Locate and identify every blood parasite.
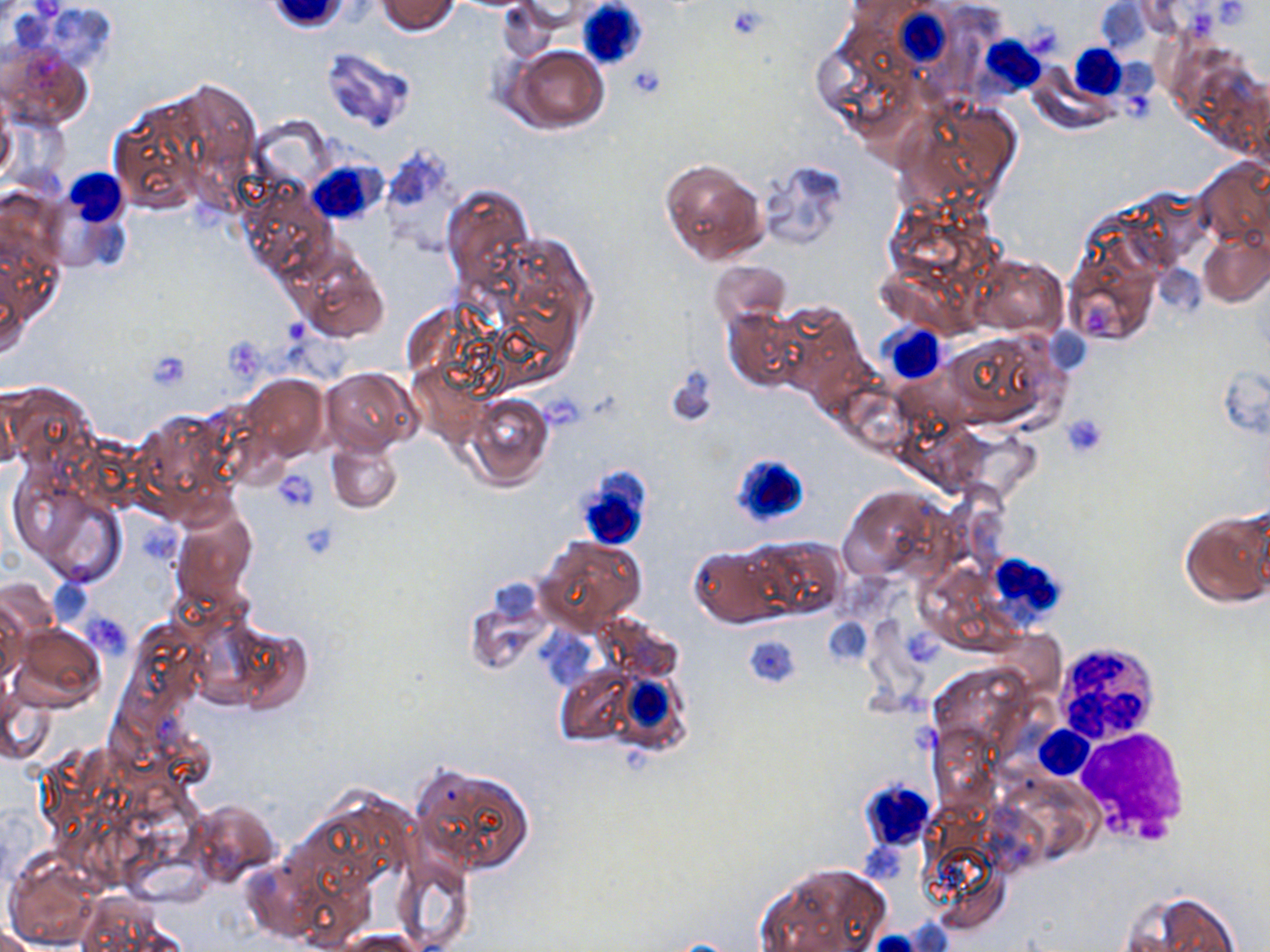
No blood parasites observed.

slide-level diagnosis = negative for blood parasites
image size = 1270×952 pixels
field of view = one of a larger specimen
platelet locations = approximate bounding boxes as (x1,y1)-(x2,y2) corner pairs in pixels: (1212,0)-(1263,29), (724,4)-(770,40), (1187,6)-(1217,38), (1022,20)-(1067,60), (626,64)-(665,101), (1085,303)-(1120,335), (277,315)-(315,346), (145,349)-(192,391), (1062,412)-(1108,456), (273,469)-(320,513)
modality = optical microscopy
white blood cell locations = approximate bounding boxes as (x1,y1)-(x2,y2) corner pairs in pixels: (578,0)-(649,70), (888,8)-(960,74), (979,36)-(1045,95), (1072,46)-(1157,99), (307,161)-(385,225), (56,167)-(131,250), (880,324)-(947,386), (731,451)-(810,537), (574,467)-(654,550), (985,552)-(1066,628), (1056,648)-(1156,743), (611,668)-(700,760), (1036,724)-(1094,779), (1074,728)-(1191,845), (858,779)-(937,854)
uninfected red blood cell locations = approximate bounding boxes as (x1,y1)-(x2,y2) corner pairs in pixels: (376,0)-(460,35), (498,0)-(566,62), (1,41)-(92,131), (508,45)-(607,135), (321,48)-(417,135), (1028,65)-(1118,134), (104,84)-(243,217), (896,100)-(1021,210), (0,104)-(17,185), (253,119)-(331,187), (380,145)-(464,251), (660,158)-(768,265), (757,159)-(847,248), (1195,159)-(1270,250), (442,184)-(534,299), (1200,228)-(1269,307), (1064,240)-(1160,345), (297,252)-(389,343), (970,255)-(1066,336), (709,261)-(791,331), (772,302)-(864,395), (724,307)-(806,392), (941,331)-(1065,431), (667,365)-(718,428), (320,368)-(419,455), (240,373)-(329,462), (0,382)-(96,470), (465,394)-(553,491), (133,408)-(240,516), (328,438)-(403,513), (30,485)-(128,587), (838,485)-(949,585), (170,505)-(257,614), (1180,507)-(1268,608), (536,535)-(646,634), (745,537)-(847,619), (689,547)-(782,627), (49,581)-(92,623), (0,593)-(25,690), (595,612)-(686,683), (11,623)-(106,714), (554,663)-(650,747), (3,685)-(56,765), (411,762)-(536,876), (188,798)-(280,884), (4,851)-(101,951), (392,851)-(474,952), (754,861)-(890,952), (1120,889)-(1246,952), (0,924)-(42,952), (338,929)-(432,952), (867,932)-(920,952)
magnification = 1000x
preparation = thin blood smear
stain = May-Grünwald-Giemsa